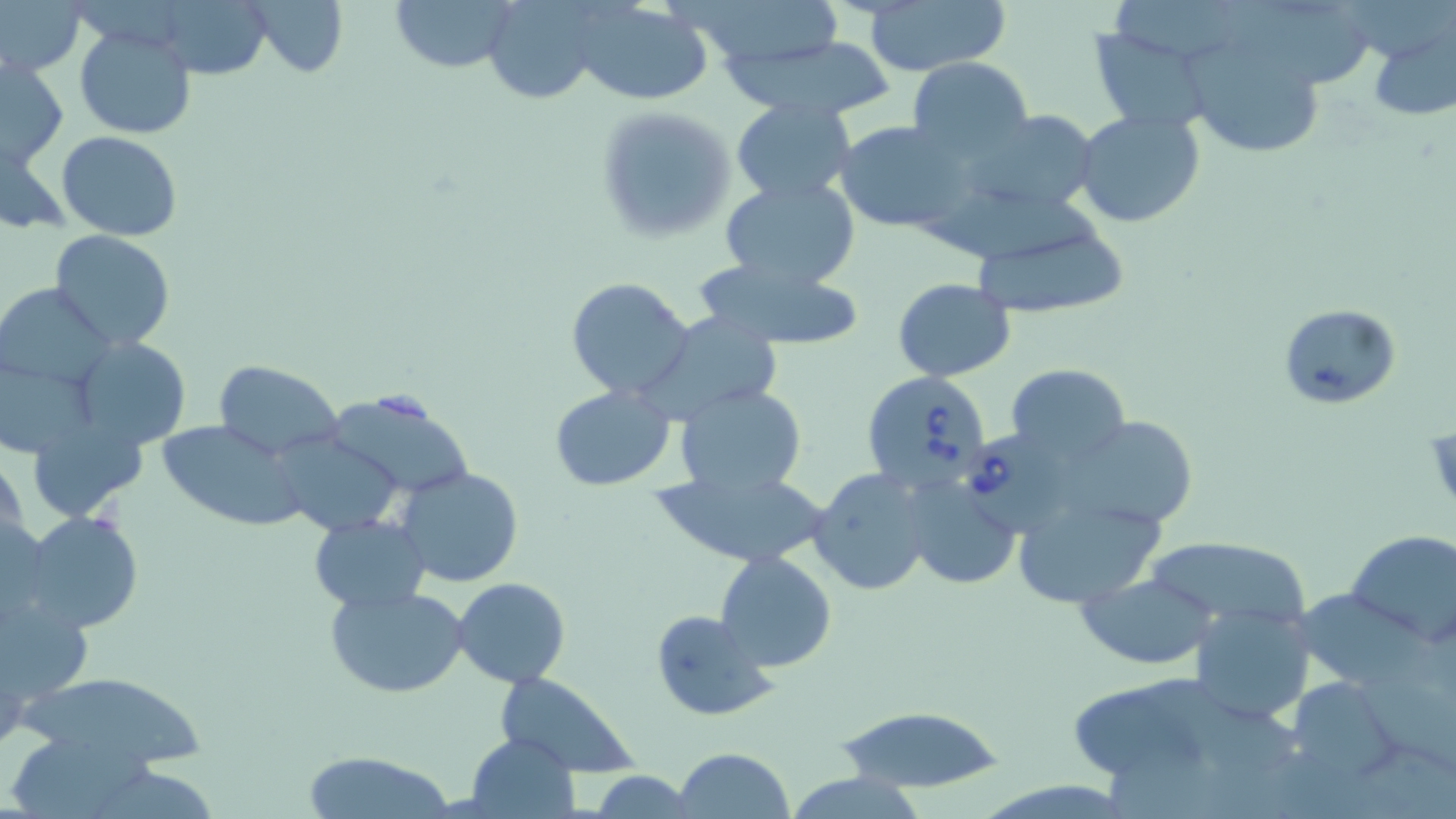
Approximate bounding boxes as [x1, y1, x2, y2] in pixels. Babesia divergens-infected red blood cell locations: [861, 369, 993, 495], [970, 424, 1095, 536]. Uninfected red blood cell locations: [251, 0, 347, 78], [387, 0, 518, 75], [480, 0, 609, 104], [675, 0, 843, 71], [1116, 0, 1252, 64], [1, 1, 87, 76], [571, 2, 712, 104], [864, 2, 1009, 76], [1228, 2, 1373, 90], [167, 4, 279, 84], [1364, 21, 1455, 124], [1084, 23, 1212, 135], [74, 24, 196, 139], [721, 34, 899, 119], [1190, 42, 1316, 163], [1, 55, 69, 168], [907, 57, 1032, 162], [731, 99, 856, 203], [594, 106, 735, 242], [1073, 108, 1206, 229], [971, 109, 1102, 215], [834, 121, 969, 233], [58, 130, 183, 238], [1, 135, 71, 233], [719, 177, 860, 290], [931, 183, 1102, 259], [966, 214, 1130, 319], [49, 230, 176, 350], [688, 257, 868, 349], [892, 276, 1018, 382], [566, 277, 696, 401], [1, 284, 113, 390], [1277, 303, 1400, 410], [640, 311, 789, 421], [70, 336, 189, 452], [210, 360, 343, 459], [1006, 363, 1130, 462], [0, 367, 104, 456], [549, 384, 675, 491], [675, 384, 806, 495], [332, 399, 474, 489], [1057, 417, 1202, 531], [38, 420, 148, 521], [159, 420, 309, 530], [275, 431, 405, 535], [0, 450, 28, 564], [808, 467, 932, 596], [398, 468, 523, 587], [659, 470, 827, 568], [902, 476, 1021, 589], [1005, 486, 1169, 609], [22, 510, 144, 635], [308, 514, 432, 611], [1347, 530, 1456, 644], [1137, 536, 1314, 630], [715, 552, 836, 673], [1075, 572, 1218, 669], [453, 577, 570, 687], [0, 582, 94, 714], [325, 584, 470, 698], [1299, 585, 1434, 685], [1193, 603, 1316, 726], [649, 609, 775, 720], [1148, 672, 1296, 772], [494, 673, 638, 777], [9, 674, 209, 765], [1288, 676, 1400, 782], [1072, 689, 1205, 777], [834, 705, 1005, 795], [464, 731, 581, 818], [11, 738, 168, 819], [1340, 740, 1456, 819], [673, 747, 796, 818], [300, 750, 456, 818], [586, 771, 699, 817]. Slide-level diagnosis: Babesia divergens. 1000x magnification. Single field of view. Image is 1456×819 pixels. May-Grünwald-Giemsa-stained preparation. Thin blood smear. Optical microscopy.